Assess for malaria.
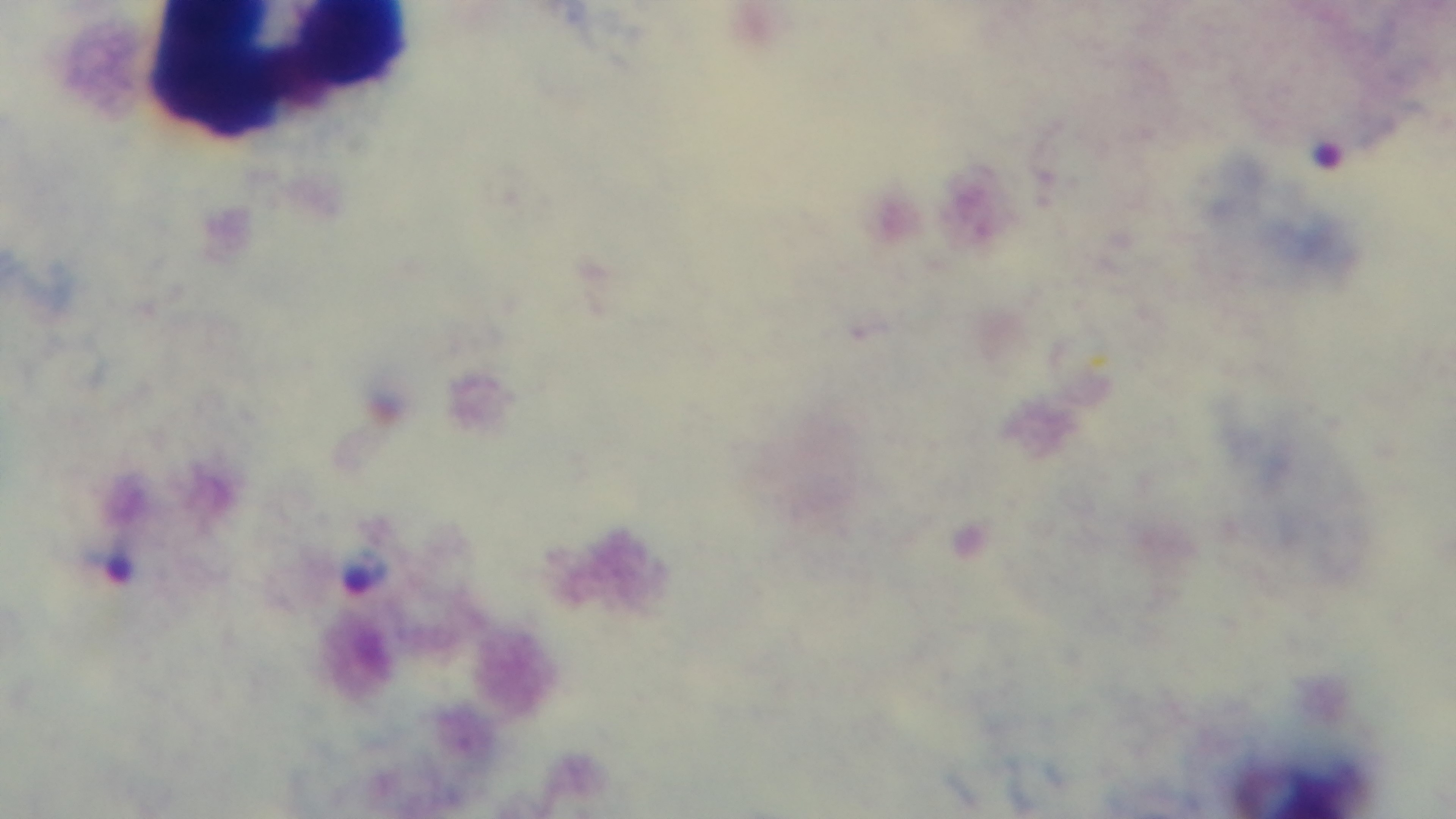
Positive.

preparation = thick
field of view = single
objective = 100x oil immersion
capture = mounted 4K digital camera
modality = light microscopy
stain = Giemsa